Identify the parasite.
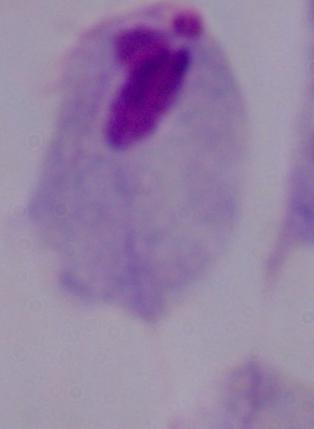

This is a trichomonad.

1000x magnification. Micrograph.